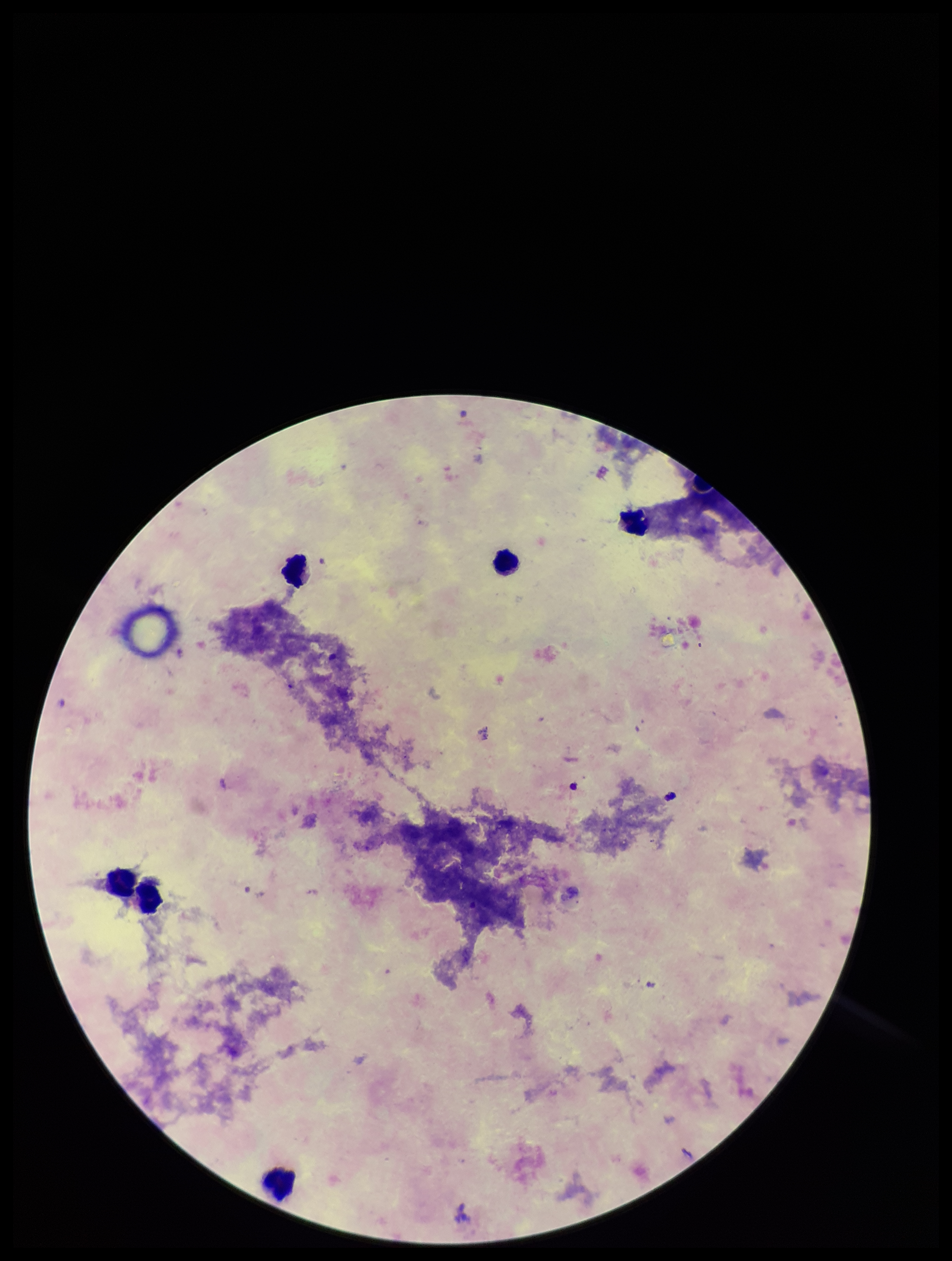
image size = 952×1261 pixels
capture = smartphone photograph through the microscope eyepiece
Plasmodium parasites = none identified
stain = Giemsa
parasite count = 0
leukocyte count = 6
field of view = single
patient malaria status = negative
preparation = thick blood smear